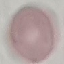

result = negative for malaria parasites
stain = Giemsa
image type = cell patch, automatically extracted from a larger field of view and resized to 64 × 64 pixels
preparation = thin blood smear
capture = smartphone through the microscope eyepiece